Classify this cell by malaria status.
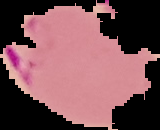
Parasitized.

Summary:
  - Image size: 160×130 pixels
  - Preparation: thin blood smear
  - Image type: segmented cell region with the area outside set to black